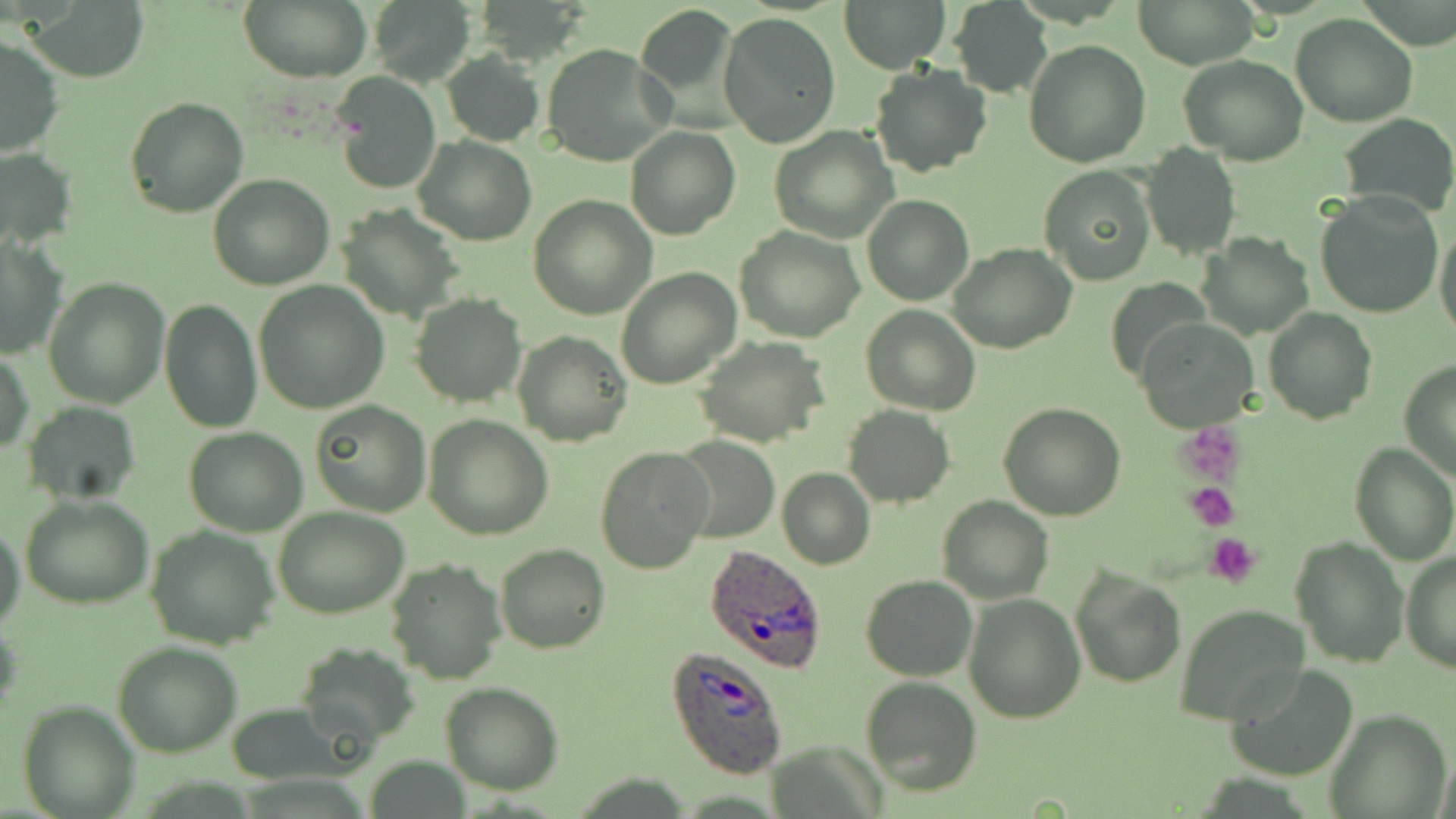

Summary:
  - Coordinate format: approximate bounding boxes as (x1,y1)-(x2,y2) corner pairs in pixels
  - Uninfected red blood cell locations: (240,0)-(371,84), (839,0)-(951,73), (1131,0)-(1257,70), (366,2)-(469,81), (950,2)-(1052,96), (26,3)-(147,81), (633,5)-(742,128), (718,13)-(840,149), (1289,14)-(1419,127), (1,33)-(65,160), (1023,41)-(1151,168), (542,44)-(674,167), (442,51)-(543,147), (1180,54)-(1308,166), (870,65)-(991,177), (332,73)-(440,195), (124,96)-(249,218), (1336,113)-(1455,220), (625,126)-(739,241), (769,126)-(897,243), (415,136)-(536,245), (1142,143)-(1240,259), (0,147)-(76,250), (1040,164)-(1156,285), (209,173)-(333,290), (1313,190)-(1443,319), (528,196)-(655,319), (862,196)-(973,305), (343,208)-(463,324), (1434,219)-(1456,344), (734,227)-(865,343), (1199,232)-(1315,339), (0,234)-(69,359), (947,243)-(1076,352), (616,267)-(741,389), (43,276)-(168,408), (252,280)-(389,413), (411,293)-(526,407), (158,297)-(263,433), (862,307)-(981,415), (1263,308)-(1376,425), (1138,320)-(1259,433), (513,329)-(631,446), (693,338)-(830,449), (1,345)-(35,454), (1399,361)-(1456,482), (311,400)-(431,517), (998,401)-(1126,520), (23,402)-(141,504), (844,404)-(954,508), (423,414)-(554,539), (183,427)-(308,536), (673,436)-(778,543), (1349,442)-(1456,564), (595,447)-(713,575), (776,466)-(875,569), (19,494)-(153,609), (938,495)-(1051,603), (274,507)-(408,619), (0,521)-(26,636), (145,526)-(279,648), (1291,536)-(1408,668), (496,543)-(610,654), (1400,550)-(1455,673), (386,559)-(505,685), (1071,566)-(1187,690), (861,574)-(978,681), (963,592)-(1085,721), (1173,604)-(1309,725), (112,641)-(242,756), (295,641)-(420,747), (1226,663)-(1359,781), (860,675)-(982,796), (440,682)-(565,795), (16,699)-(139,819), (1328,711)-(1451,817)
  - Plasmodium ovale-infected red blood cell locations: (702,545)-(832,672), (667,646)-(791,778)
  - Platelet locations: (1178,427)-(1243,483), (1186,483)-(1239,530), (1204,532)-(1262,587)
  - Slide-level diagnosis: Plasmodium ovale
  - Preparation: thin blood smear
  - Magnification: 1000x
  - Stain: May-Grünwald-Giemsa
  - Field of view: single
  - Modality: optical microscopy
  - Image size: 1456×819 pixels